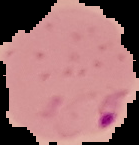

preparation = thin blood smear
result = Plasmodium parasites identified
image size = 139×145 pixels
image type = cell region segmented out of the field of view; surrounding area masked to black